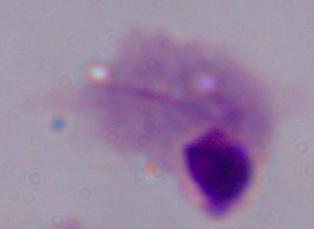

magnification = 1000x
identification = trichomonad
modality = photomicrograph